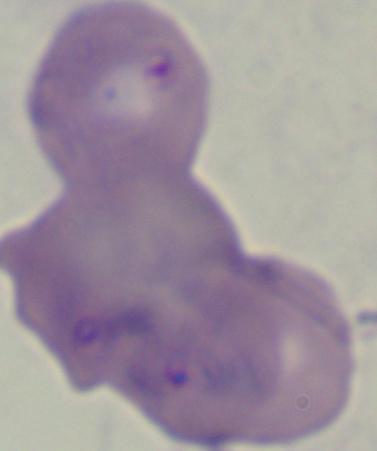
Summary:
  - Identification: Babesia
  - Magnification: 1000x
  - Modality: photomicrograph